Locate every blood parasite and identify its species.
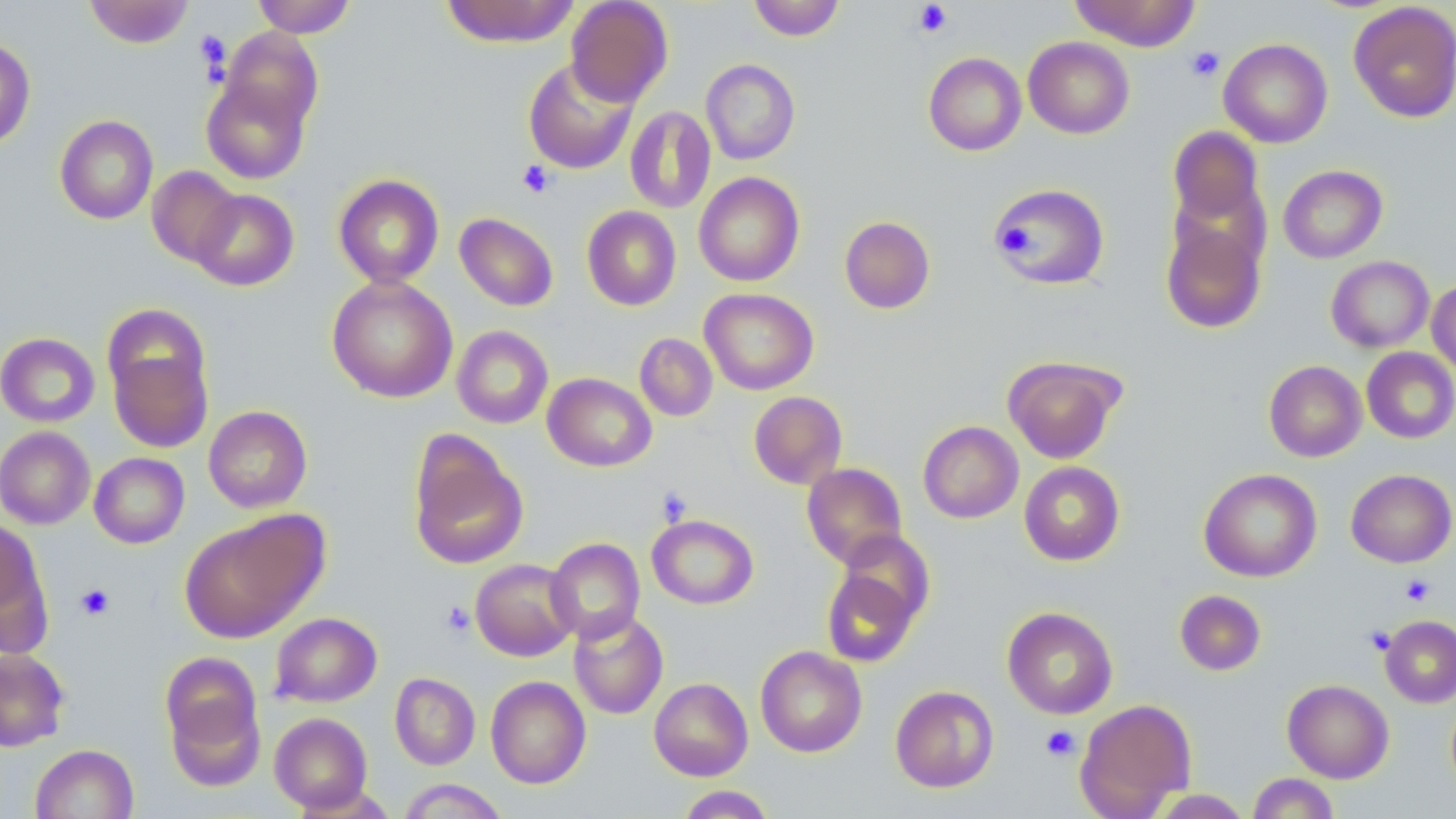

No blood parasites observed.

{
  "slide_level_diagnosis": "no evidence of blood parasites",
  "modality": "optical microscopy",
  "field_of_view": "single",
  "platelet_locations": "approximate bounding boxes as named x1/y1/x2/y2 corners in pixels: (x1=913, y1=1, x2=953, y2=37), (x1=195, y1=31, x2=231, y2=78), (x1=1185, y1=46, x2=1224, y2=82), (x1=518, y1=160, x2=555, y2=198), (x1=996, y1=222, x2=1039, y2=257), (x1=655, y1=487, x2=693, y2=526), (x1=1400, y1=574, x2=1435, y2=606), (x1=76, y1=584, x2=115, y2=620), (x1=441, y1=600, x2=476, y2=637), (x1=1040, y1=725, x2=1080, y2=762)",
  "magnification": "1000x",
  "uninfected_red_blood_cell_locations": "approximate bounding boxes as named x1/y1/x2/y2 corners in pixels: (x1=84, y1=0, x2=195, y2=48), (x1=252, y1=0, x2=356, y2=38), (x1=440, y1=0, x2=580, y2=47), (x1=565, y1=0, x2=673, y2=108), (x1=748, y1=0, x2=845, y2=41), (x1=1069, y1=0, x2=1201, y2=51), (x1=1348, y1=2, x2=1456, y2=123), (x1=220, y1=27, x2=323, y2=133), (x1=1023, y1=36, x2=1134, y2=139), (x1=0, y1=37, x2=36, y2=150), (x1=1219, y1=38, x2=1333, y2=148), (x1=923, y1=52, x2=1026, y2=156), (x1=522, y1=58, x2=638, y2=174), (x1=701, y1=59, x2=800, y2=165), (x1=201, y1=74, x2=312, y2=184), (x1=625, y1=105, x2=716, y2=214), (x1=55, y1=114, x2=158, y2=224), (x1=1168, y1=126, x2=1264, y2=227), (x1=1278, y1=164, x2=1387, y2=263), (x1=147, y1=166, x2=243, y2=267), (x1=693, y1=172, x2=804, y2=287), (x1=333, y1=174, x2=444, y2=288), (x1=991, y1=181, x2=1110, y2=290), (x1=191, y1=189, x2=299, y2=291), (x1=582, y1=206, x2=682, y2=310), (x1=1160, y1=211, x2=1268, y2=335), (x1=454, y1=212, x2=559, y2=311), (x1=839, y1=216, x2=935, y2=314), (x1=1326, y1=256, x2=1434, y2=353), (x1=326, y1=275, x2=458, y2=403), (x1=1427, y1=278, x2=1456, y2=378), (x1=699, y1=288, x2=819, y2=395), (x1=451, y1=325, x2=554, y2=429), (x1=0, y1=332, x2=100, y2=427), (x1=635, y1=333, x2=718, y2=421), (x1=106, y1=336, x2=214, y2=456), (x1=1361, y1=347, x2=1456, y2=444), (x1=1003, y1=356, x2=1123, y2=463), (x1=1264, y1=360, x2=1366, y2=462), (x1=542, y1=373, x2=657, y2=472), (x1=748, y1=391, x2=847, y2=489), (x1=203, y1=405, x2=312, y2=513), (x1=918, y1=421, x2=1023, y2=523), (x1=0, y1=426, x2=95, y2=529), (x1=407, y1=433, x2=529, y2=570), (x1=89, y1=452, x2=189, y2=548), (x1=1019, y1=461, x2=1125, y2=566), (x1=802, y1=462, x2=907, y2=567), (x1=1199, y1=468, x2=1322, y2=582), (x1=1345, y1=468, x2=1456, y2=568), (x1=179, y1=514, x2=322, y2=643), (x1=646, y1=514, x2=759, y2=609), (x1=0, y1=518, x2=49, y2=641), (x1=835, y1=532, x2=935, y2=629), (x1=545, y1=537, x2=645, y2=644), (x1=471, y1=559, x2=578, y2=661), (x1=821, y1=565, x2=921, y2=667), (x1=1175, y1=589, x2=1266, y2=675), (x1=1002, y1=606, x2=1118, y2=719), (x1=569, y1=609, x2=668, y2=720), (x1=270, y1=612, x2=382, y2=707), (x1=1380, y1=615, x2=1456, y2=708), (x1=755, y1=645, x2=867, y2=757), (x1=0, y1=649, x2=70, y2=751), (x1=161, y1=653, x2=266, y2=780), (x1=389, y1=672, x2=480, y2=770), (x1=486, y1=675, x2=591, y2=789), (x1=649, y1=677, x2=753, y2=781), (x1=1282, y1=679, x2=1394, y2=783), (x1=890, y1=685, x2=999, y2=793), (x1=1074, y1=699, x2=1196, y2=817), (x1=269, y1=712, x2=373, y2=813), (x1=30, y1=743, x2=138, y2=818), (x1=1247, y1=773, x2=1340, y2=818), (x1=398, y1=779, x2=509, y2=819), (x1=674, y1=785, x2=778, y2=818), (x1=1148, y1=789, x2=1254, y2=818)",
  "preparation": "thin blood smear",
  "stain": "May-Grünwald-Giemsa",
  "image_size": "1456×819 pixels"
}